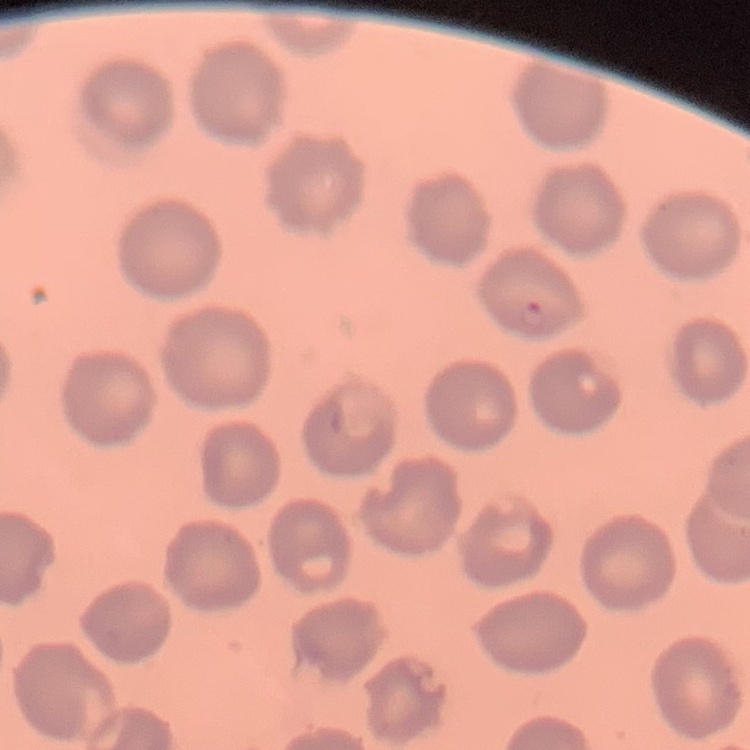
The red blood cells exhibit no rouleaux formation. One tile cut from a larger photomicrograph. Field's or Giemsa stain. Thin blood smear.